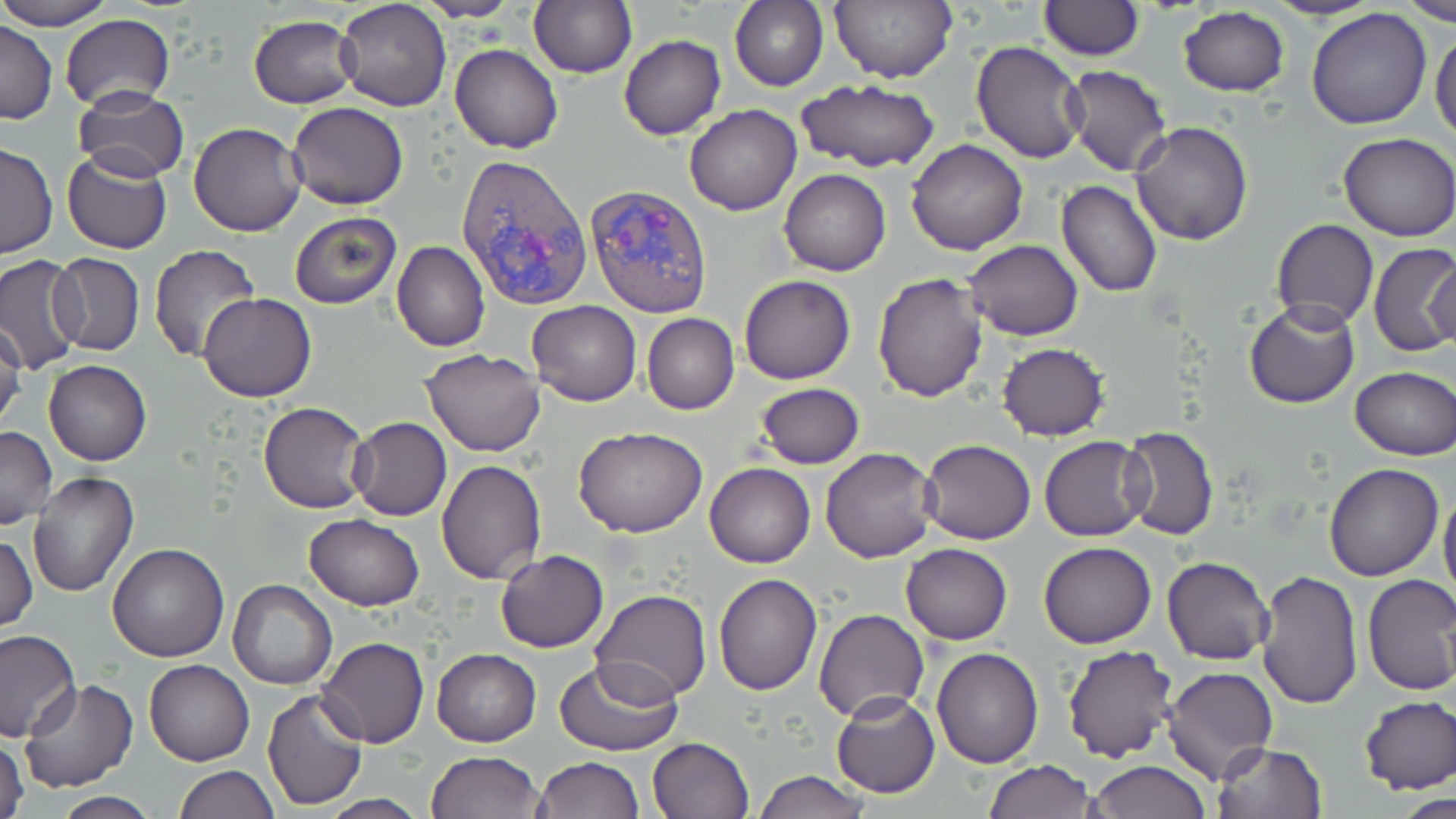

Summary:
  - Coordinate format: approximate bounding boxes as (x1,y1)-(x2,y2) corner pairs in pixels
  - Plasmodium vivax-infected red blood cell locations: (456,154)-(593,310), (585,182)-(713,319)
  - Uninfected red blood cell locations: (0,0)-(118,29), (415,0)-(518,21), (529,0)-(636,78), (831,0)-(956,84), (1267,0)-(1382,21), (1397,0)-(1456,24), (335,1)-(451,112), (731,1)-(827,91), (1037,1)-(1143,59), (1176,6)-(1291,97), (1305,8)-(1433,130), (59,14)-(175,112), (248,16)-(361,108), (0,21)-(57,124), (1430,26)-(1455,144), (619,34)-(726,139), (970,41)-(1089,164), (450,43)-(564,154), (1064,65)-(1172,176), (794,78)-(941,174), (74,88)-(188,182), (286,102)-(408,209), (684,104)-(802,215), (1131,120)-(1254,246), (189,122)-(306,236), (1337,133)-(1456,240), (906,139)-(1029,255), (0,142)-(57,260), (62,150)-(172,254), (778,169)-(890,276), (1055,179)-(1163,298), (289,212)-(402,309), (1270,219)-(1378,332), (965,240)-(1083,341), (1369,241)-(1456,358), (393,242)-(490,351), (148,245)-(260,361), (46,253)-(143,357), (0,255)-(86,373), (1426,257)-(1455,353), (873,272)-(989,402), (738,275)-(855,385), (198,294)-(316,402), (527,300)-(642,405), (1244,301)-(1361,409), (641,313)-(739,415), (0,322)-(27,435), (997,343)-(1108,440), (420,349)-(546,457), (44,360)-(151,467), (1350,366)-(1456,458), (755,383)-(865,468), (257,401)-(372,514), (348,417)-(452,521), (0,425)-(56,530), (1120,425)-(1220,539), (572,426)-(707,537), (1039,435)-(1150,541), (919,438)-(1036,544), (820,448)-(939,562), (437,458)-(546,583), (704,462)-(815,567), (1323,462)-(1445,581), (27,471)-(138,596), (1439,485)-(1456,603), (303,514)-(425,609), (1,533)-(37,634), (1039,540)-(1156,649), (107,542)-(230,661), (899,543)-(1013,645), (495,549)-(609,653), (1162,556)-(1274,665), (1255,569)-(1363,710), (713,572)-(823,694), (1361,574)-(1456,696), (227,578)-(337,690), (589,590)-(712,704), (813,608)-(930,724), (0,630)-(81,743), (316,638)-(429,748), (931,645)-(1044,768), (1063,645)-(1179,763), (432,648)-(540,746), (144,659)-(254,767), (554,660)-(684,755), (1160,666)-(1280,785), (19,680)-(138,793), (263,689)-(367,811), (832,691)-(940,798), (1358,695)-(1456,794), (647,736)-(755,819), (1,738)-(30,819), (1213,743)-(1327,819), (426,750)-(544,819), (533,756)-(643,818), (985,760)-(1095,818), (1088,760)-(1210,819), (174,765)-(280,818), (755,771)-(871,818), (1402,791)-(1456,819), (52,793)-(162,819), (318,796)-(432,818)
  - Slide-level diagnosis: Plasmodium vivax
  - Magnification: 1000x
  - Stain: May-Grünwald-Giemsa
  - Field of view: one of a larger specimen
  - Image size: 1456×819 pixels
  - Preparation: thin blood film
  - Modality: light microscopy